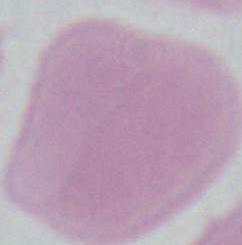

A red blood cell is seen. 1000x magnification. Photomicrograph.